Name the parasite shown.
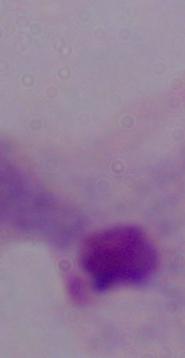
This is a trichomonad.

modality = micrograph
magnification = 1000x